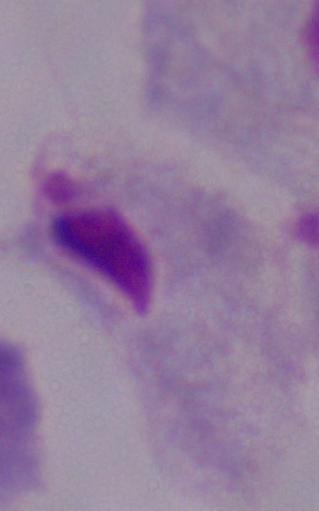
Captured at 1000x magnification. Photomicrograph. A trichomonad is seen.